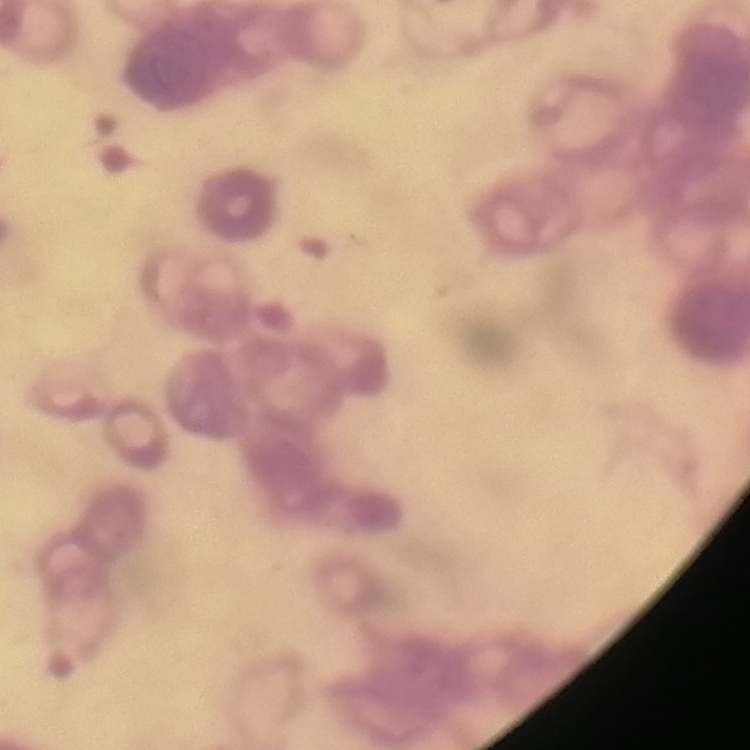
erythrocyte morphology = rouleaux formation
stain = Field's or Giemsa
preparation = thin blood film
image type = one tile cut from a larger photomicrograph